Comment on the morphology of the erythrocytes.
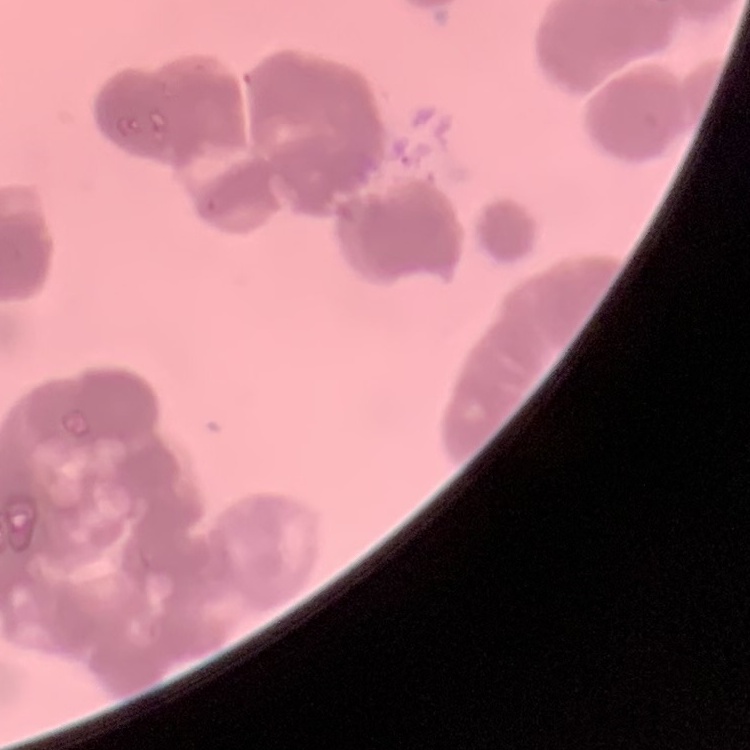

They show rouleaux formation.

preparation: thin blood smear
image_type: one tile cut from a larger photomicrograph
stain: Field's or Giemsa